Comment on the morphology of the red blood cells.
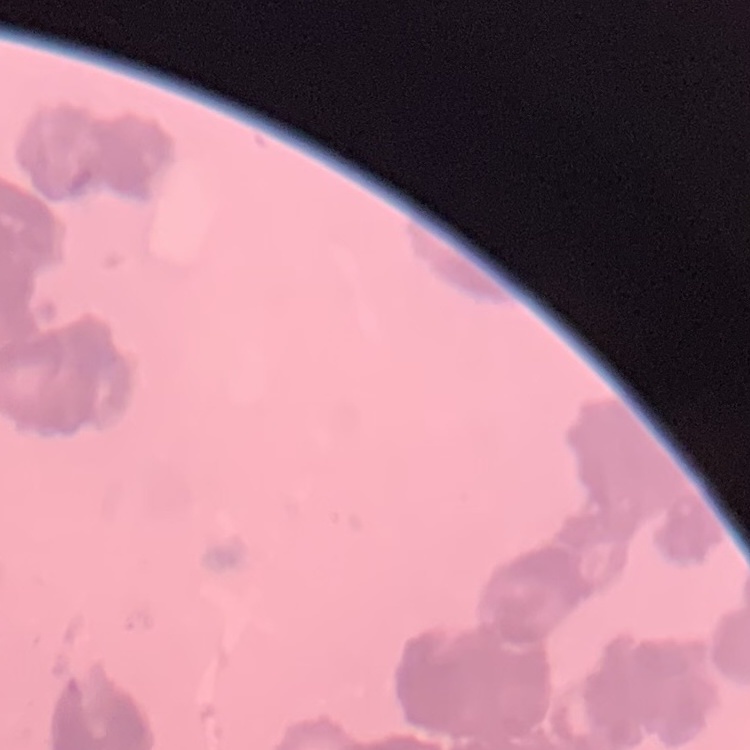
They show rouleaux formation.

Thin peripheral smear. One tile cut from a larger photomicrograph. Field's or Giemsa stain.